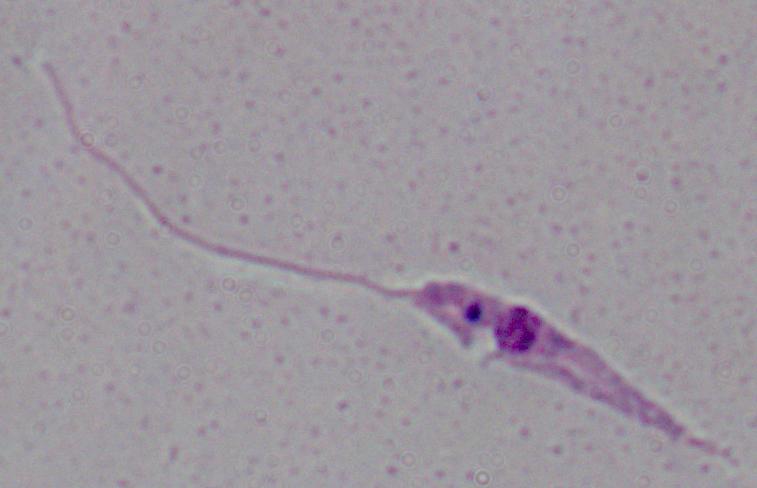
Summary:
  - Magnification: 1000x
  - Modality: micrograph
  - Identification: Leishmania